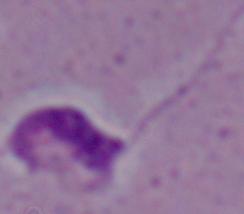
magnification: 1000x
identification: Leishmania
modality: micrograph